Report the malaria status of this cell.
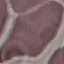
It is uninfected.

stain = Giemsa
preparation = thin smear
image type = cell patch, automatically extracted from a larger field of view and resized to 64 × 64 pixels
capture = smartphone camera at the microscope eyepiece